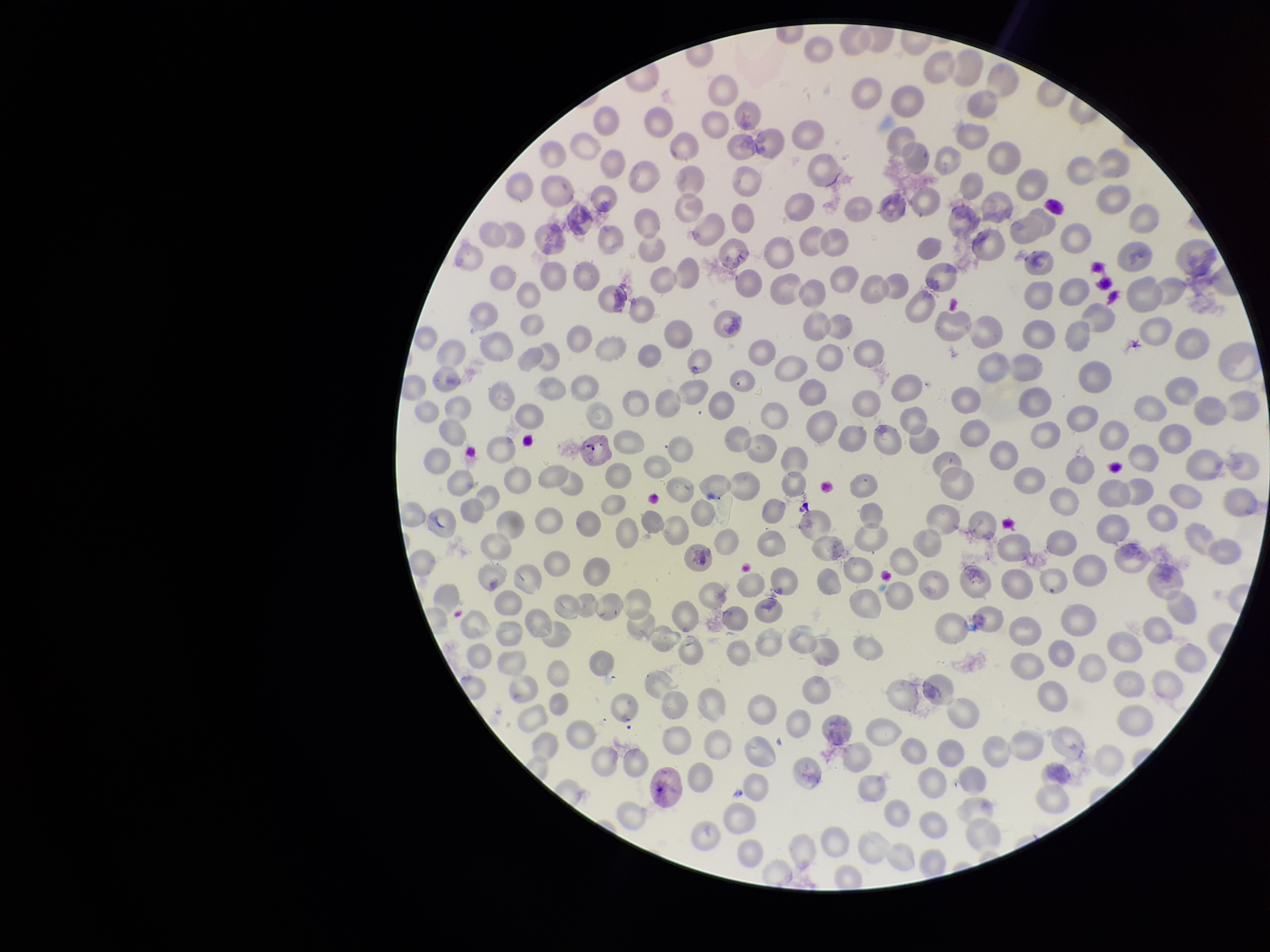
Patient malaria status: infected. Species reported for this patient: Plasmodium vivax. Image is 1270×952 pixels. One field from this slide. Red blood cell count: 279. Preparation: thin blood smear. Smartphone photograph taken through the eyepiece of a microscope. Parasitized red blood cell count: 1. Stained with Giemsa. Parasitized red blood cells: detected.